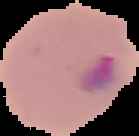 Result: malaria parasites detected. Cell region segmented out of the field of view; the surrounding area is masked to black. From a thin blood film. Image is 139×136 pixels.